Classify this cell by malaria status.
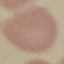
Uninfected.

stain: Giemsa
image_type: automatically extracted cell patch, resized to 64 × 64 pixels
capture: smartphone camera at the microscope eyepiece
preparation: thin blood film